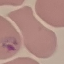

{
  "malaria_status": "parasitized",
  "image_type": "cell patch, automatically extracted from a larger field of view and resized to 64 × 64 pixels",
  "capture": "smartphone camera at the microscope eyepiece",
  "preparation": "thin blood smear",
  "stain": "Giemsa"
}